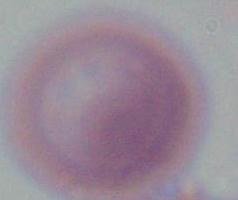

magnification: 1000x
identification: red blood cell
modality: micrograph